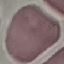

result = no malaria parasites detected
capture = smartphone camera at the microscope eyepiece
preparation = thin blood smear
image type = cell patch, automatically extracted from a larger field of view and resized to 64 × 64 pixels
stain = Giemsa